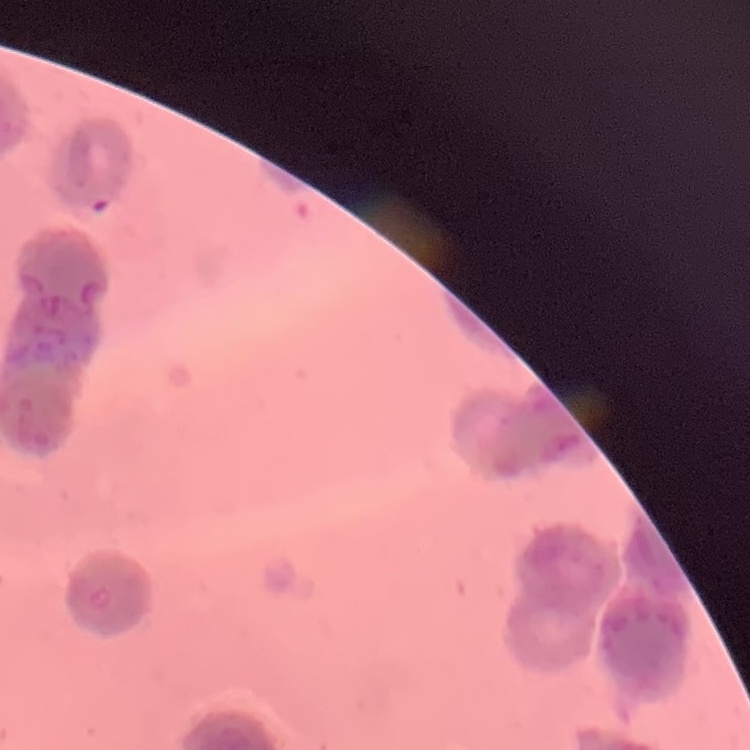
The erythrocytes exhibit rouleaux formation. Thin blood smear. One tile cut from a larger photomicrograph. Field's or Giemsa stain.